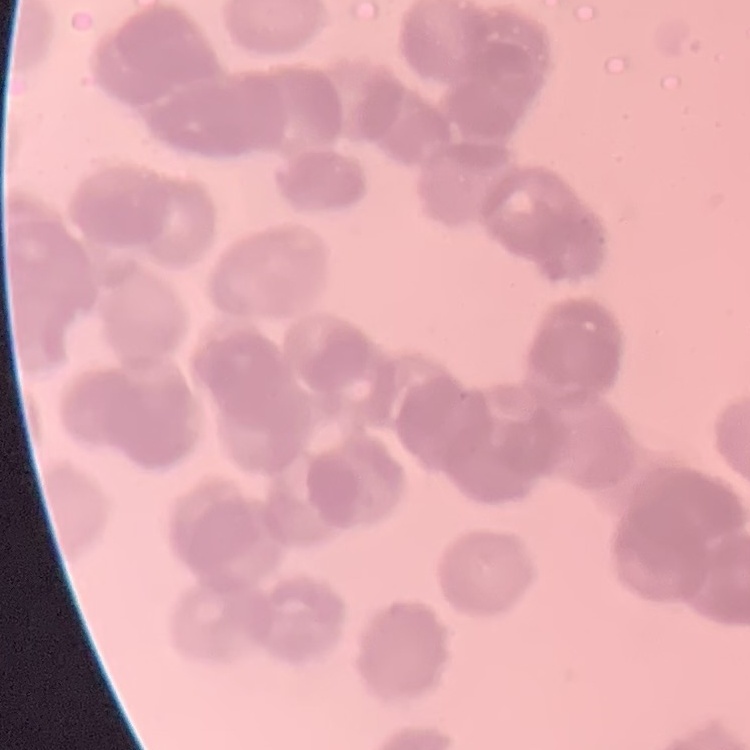
Summary:
  - Erythrocyte morphology: rouleaux formation
  - Stain: Field's or Giemsa
  - Preparation: thin peripheral smear
  - Image type: square crop of a larger photomicrograph